Outline each blood parasite and name the species.
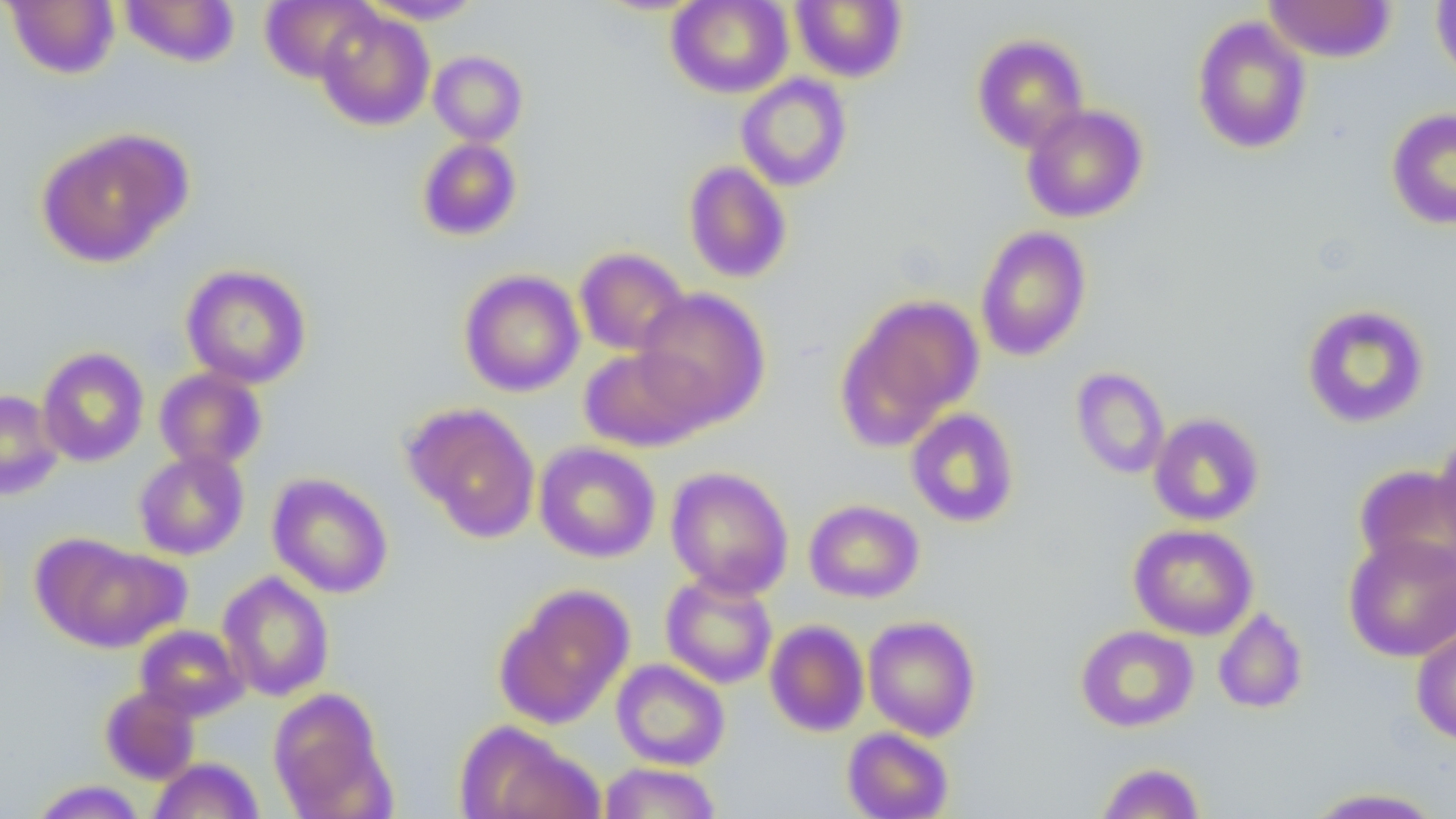

No blood parasites seen.

Summary:
  - Coordinate format: approximate bounding boxes as (x1, y1, x2, y2) in pixels
  - Uninfected red blood cell locations: (4, 0, 121, 79), (119, 0, 240, 67), (260, 0, 378, 83), (360, 0, 485, 25), (666, 0, 793, 98), (791, 0, 907, 82), (1263, 0, 1396, 63), (1431, 0, 1456, 85), (315, 9, 435, 131), (1191, 16, 1312, 155), (972, 34, 1089, 153), (429, 50, 527, 146), (736, 74, 853, 192), (1021, 104, 1148, 223), (1386, 108, 1456, 229), (36, 127, 192, 268), (417, 138, 522, 240), (683, 161, 792, 283), (975, 225, 1092, 361), (575, 247, 690, 357), (180, 264, 312, 388), (459, 270, 585, 396), (634, 287, 771, 427), (838, 294, 983, 441), (1301, 304, 1430, 429), (37, 346, 149, 467), (579, 346, 711, 451), (1070, 366, 1170, 479), (154, 367, 267, 471), (0, 389, 64, 500), (404, 403, 540, 541), (905, 408, 1020, 527), (1148, 413, 1265, 526), (1432, 431, 1456, 553), (533, 441, 661, 563), (133, 450, 249, 560), (1354, 465, 1456, 580), (665, 466, 794, 598), (267, 473, 393, 599), (804, 499, 925, 603), (1128, 523, 1259, 640), (1343, 534, 1456, 662), (36, 537, 186, 652), (217, 571, 335, 701), (660, 572, 778, 689), (496, 584, 635, 730), (1213, 607, 1308, 714), (863, 615, 981, 741), (765, 619, 870, 737), (134, 624, 248, 721), (1076, 624, 1199, 732), (1411, 626, 1456, 746), (611, 659, 730, 770), (100, 686, 200, 784), (268, 688, 389, 814), (455, 721, 600, 819), (842, 727, 954, 819), (148, 757, 264, 818), (1095, 761, 1206, 818), (599, 762, 722, 819), (29, 780, 148, 819), (1301, 787, 1447, 818)
  - Slide-level diagnosis: no evidence of blood parasites
  - Magnification: 1000x
  - Modality: optical microscopy
  - Preparation: thin blood film
  - Image size: 1456×819 pixels
  - Field of view: single